Locate every leukocyte (white blood cell).
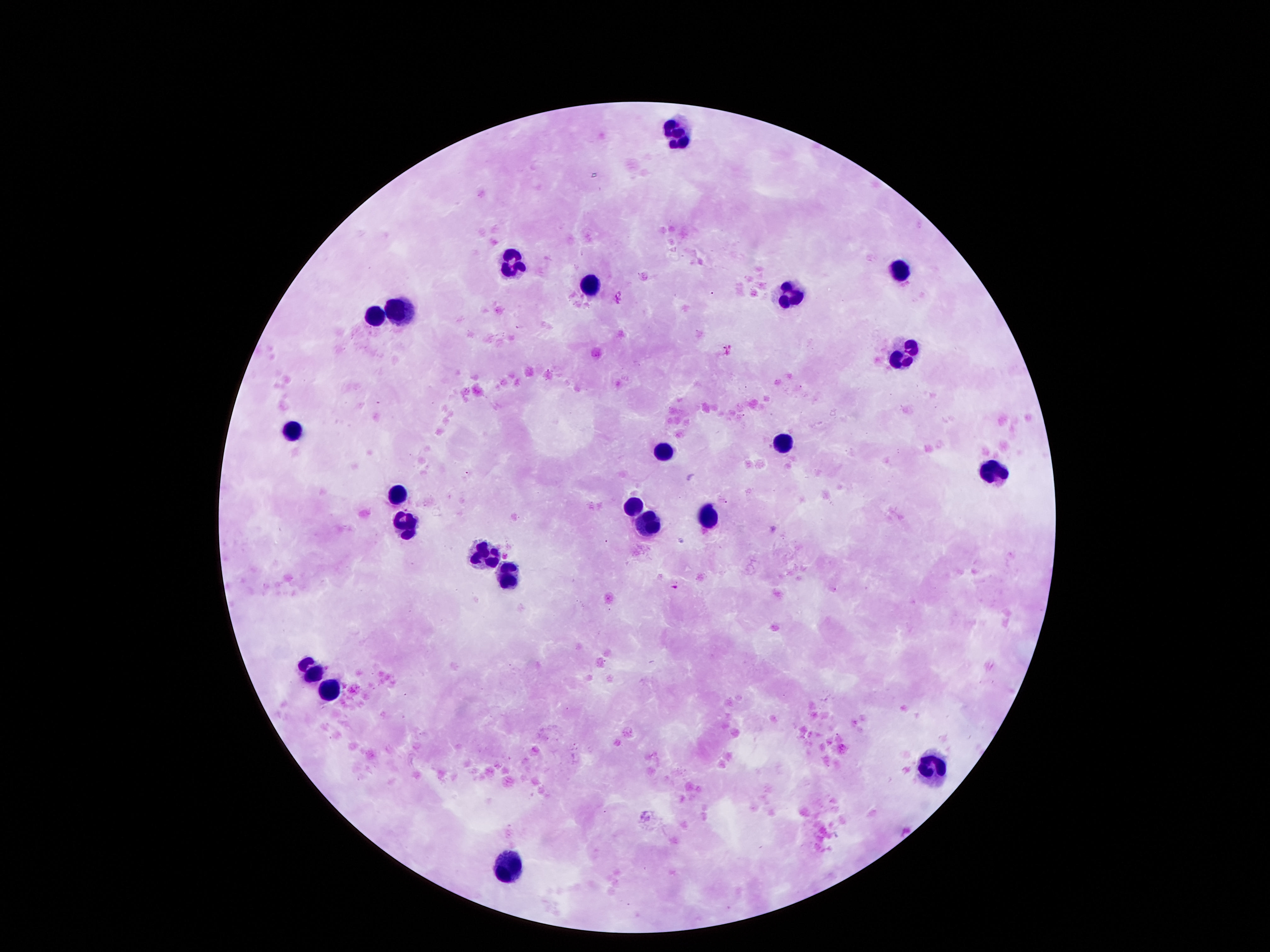

Approximate centers as {x, y} in pixels.
Leukocytes: {678, 135}, {504, 268}, {898, 270}, {591, 283}, {791, 291}, {397, 312}, {374, 314}, {904, 349}, {290, 431}, {788, 439}, {664, 450}, {991, 470}, {394, 494}, {635, 505}, {704, 515}, {649, 520}, {403, 523}, {481, 546}, {507, 574}, {304, 668}, {325, 690}, {936, 766}, {504, 861}.

preparation = thick blood film
field of view = single
magnification = 100x
stain = Giemsa
capture = smartphone camera through the microscope eyepiece
image size = 1270×952 pixels
patient malaria status = uninfected